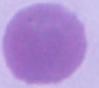 A red blood cell is shown. Captured at 1000x magnification. Micrograph.